Give the position of every Plasmodium parasite.
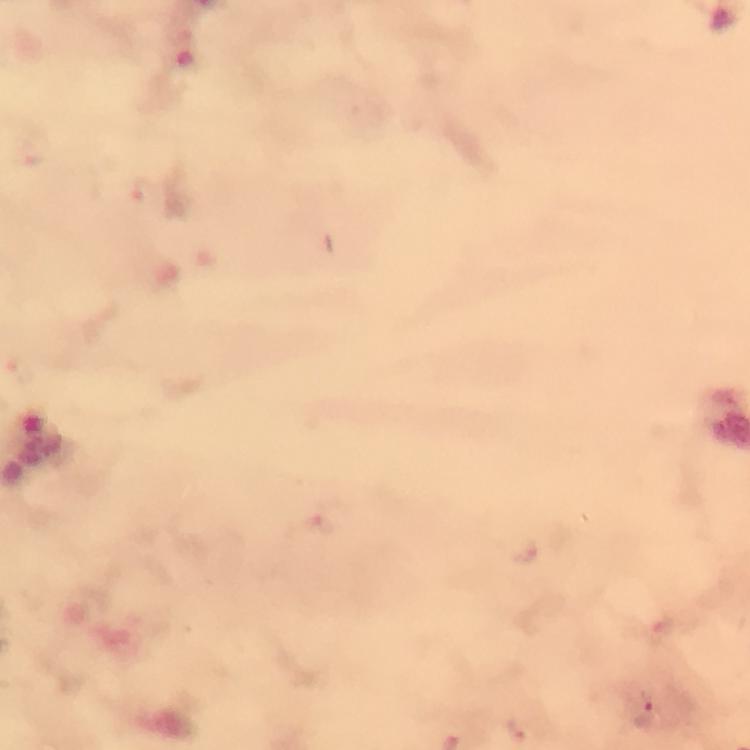
Approximate centers as (x, y) in pixels.
Plasmodium parasites: (318, 523), (524, 551), (642, 711), (517, 729).

stain = Giemsa
capture = smartphone camera through the microscope
cropped from = a single field of view
context = from a malaria diagnostic workup
magnification = 100x
preparation = thick smear
image size = 750×750 pixels
immersion oil = applied